State which cell type is depicted.
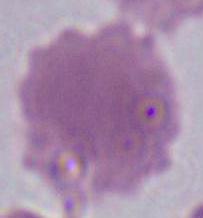

This is an erythrocyte.

Captured at 1000x magnification. Photomicrograph.